Locate and identify every blood parasite.
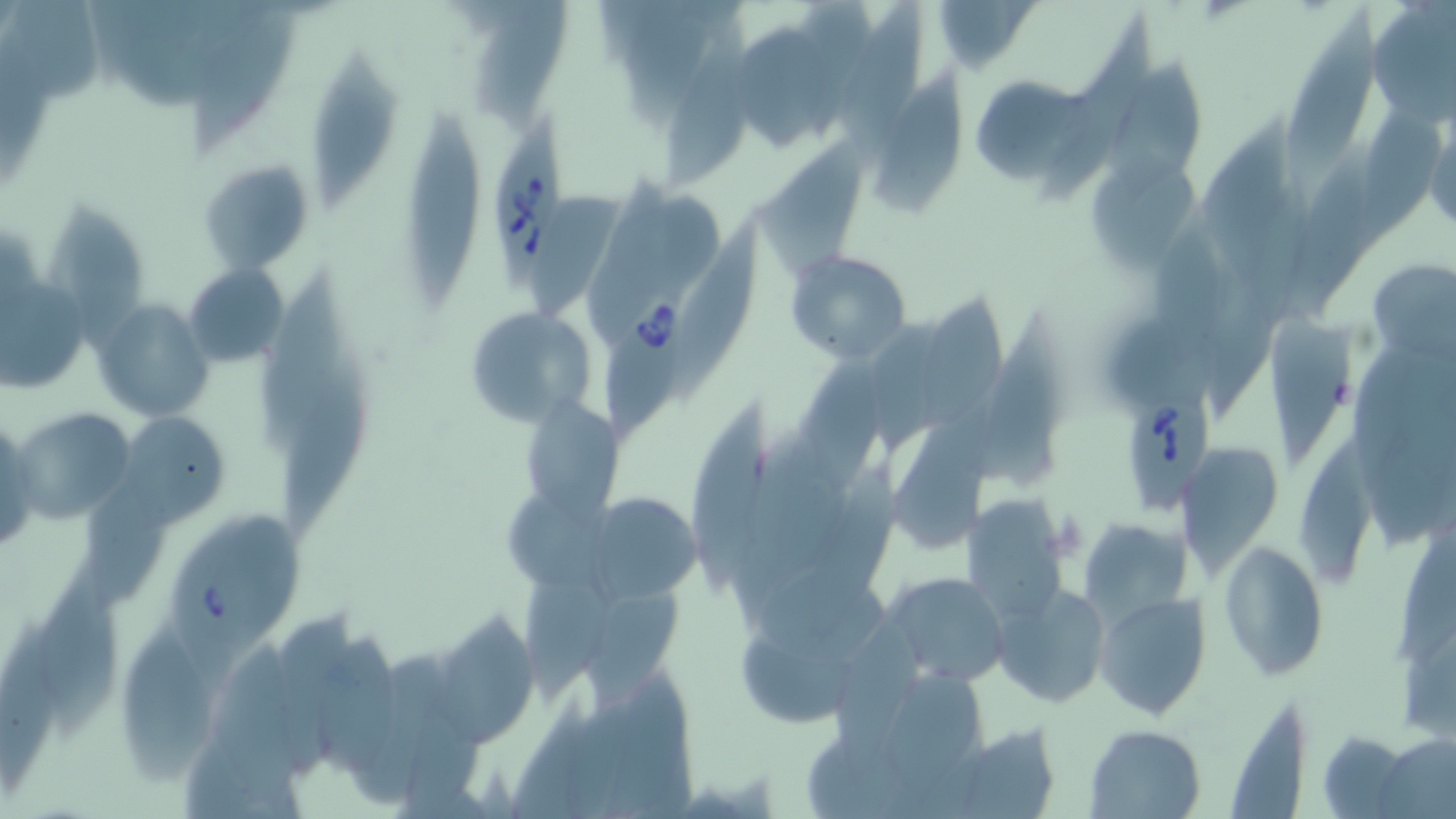

Approximate bounding boxes as named x1/y1/x2/y2 corners in pixels.
Babesia divergens-infected red blood cells: (x1=493, y1=109, x2=569, y2=291), (x1=595, y1=278, x2=694, y2=455), (x1=1116, y1=394, x2=1209, y2=513), (x1=158, y1=505, x2=314, y2=693).
No Plasmodium falciparum, Plasmodium ovale, Plasmodium malariae, Plasmodium vivax, or Trypanosoma brucei observed.

{
  "slide_level_diagnosis": "Babesia divergens",
  "stain": "May-Grünwald-Giemsa",
  "image_size": "1456×819 pixels",
  "magnification": "1000x",
  "preparation": "thin blood film",
  "uninfected_red_blood_cell_locations": "approximate bounding boxes as named x1/y1/x2/y2 corners in pixels: (x1=1366, y1=0, x2=1456, y2=121), (x1=8, y1=3, x2=108, y2=111), (x1=188, y1=3, x2=299, y2=158), (x1=478, y1=3, x2=574, y2=132), (x1=1285, y1=3, x2=1383, y2=196), (x1=830, y1=5, x2=927, y2=154), (x1=1041, y1=12, x2=1171, y2=208), (x1=663, y1=24, x2=751, y2=193), (x1=735, y1=27, x2=839, y2=152), (x1=310, y1=51, x2=401, y2=209), (x1=1111, y1=57, x2=1211, y2=194), (x1=870, y1=70, x2=969, y2=215), (x1=979, y1=74, x2=1090, y2=188), (x1=397, y1=106, x2=484, y2=306), (x1=1423, y1=113, x2=1455, y2=234), (x1=751, y1=137, x2=883, y2=282), (x1=1292, y1=147, x2=1381, y2=318), (x1=198, y1=160, x2=315, y2=275), (x1=1086, y1=162, x2=1201, y2=275), (x1=535, y1=192, x2=626, y2=314), (x1=45, y1=206, x2=151, y2=356), (x1=675, y1=224, x2=768, y2=397), (x1=786, y1=251, x2=911, y2=364), (x1=1366, y1=258, x2=1456, y2=363), (x1=185, y1=263, x2=289, y2=367), (x1=255, y1=268, x2=352, y2=452), (x1=1, y1=274, x2=94, y2=391), (x1=922, y1=296, x2=1014, y2=428), (x1=93, y1=300, x2=216, y2=421), (x1=462, y1=306, x2=598, y2=428), (x1=1267, y1=315, x2=1353, y2=466), (x1=977, y1=324, x2=1067, y2=492), (x1=798, y1=350, x2=894, y2=494), (x1=281, y1=367, x2=369, y2=534), (x1=896, y1=404, x2=999, y2=554), (x1=689, y1=405, x2=779, y2=602), (x1=522, y1=406, x2=624, y2=521), (x1=13, y1=412, x2=138, y2=528), (x1=120, y1=412, x2=229, y2=525), (x1=0, y1=419, x2=39, y2=561), (x1=1174, y1=439, x2=1285, y2=575), (x1=1303, y1=444, x2=1383, y2=583), (x1=506, y1=492, x2=622, y2=595), (x1=592, y1=493, x2=707, y2=609), (x1=959, y1=497, x2=1070, y2=626), (x1=1081, y1=520, x2=1190, y2=628), (x1=1389, y1=531, x2=1456, y2=673), (x1=1217, y1=540, x2=1329, y2=680), (x1=39, y1=555, x2=130, y2=743), (x1=757, y1=565, x2=895, y2=658), (x1=515, y1=572, x2=617, y2=696), (x1=879, y1=573, x2=1011, y2=688), (x1=992, y1=583, x2=1112, y2=710), (x1=1096, y1=591, x2=1210, y2=719), (x1=0, y1=611, x2=73, y2=797), (x1=433, y1=612, x2=539, y2=746), (x1=833, y1=622, x2=929, y2=791), (x1=740, y1=624, x2=860, y2=727), (x1=120, y1=626, x2=214, y2=797), (x1=313, y1=633, x2=406, y2=783), (x1=214, y1=638, x2=307, y2=818), (x1=1228, y1=707, x2=1309, y2=818), (x1=938, y1=723, x2=1063, y2=819), (x1=1085, y1=725, x2=1205, y2=817), (x1=1316, y1=731, x2=1412, y2=817), (x1=1371, y1=733, x2=1455, y2=819)",
  "field_of_view": "single",
  "modality": "optical microscopy"
}